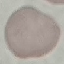

Malaria status: uninfected. Cell patch, automatically extracted from a larger field of view and resized to 64 × 64 pixels. Acquired by smartphone through the microscope eyepiece. Thin blood smear. Giemsa stain.